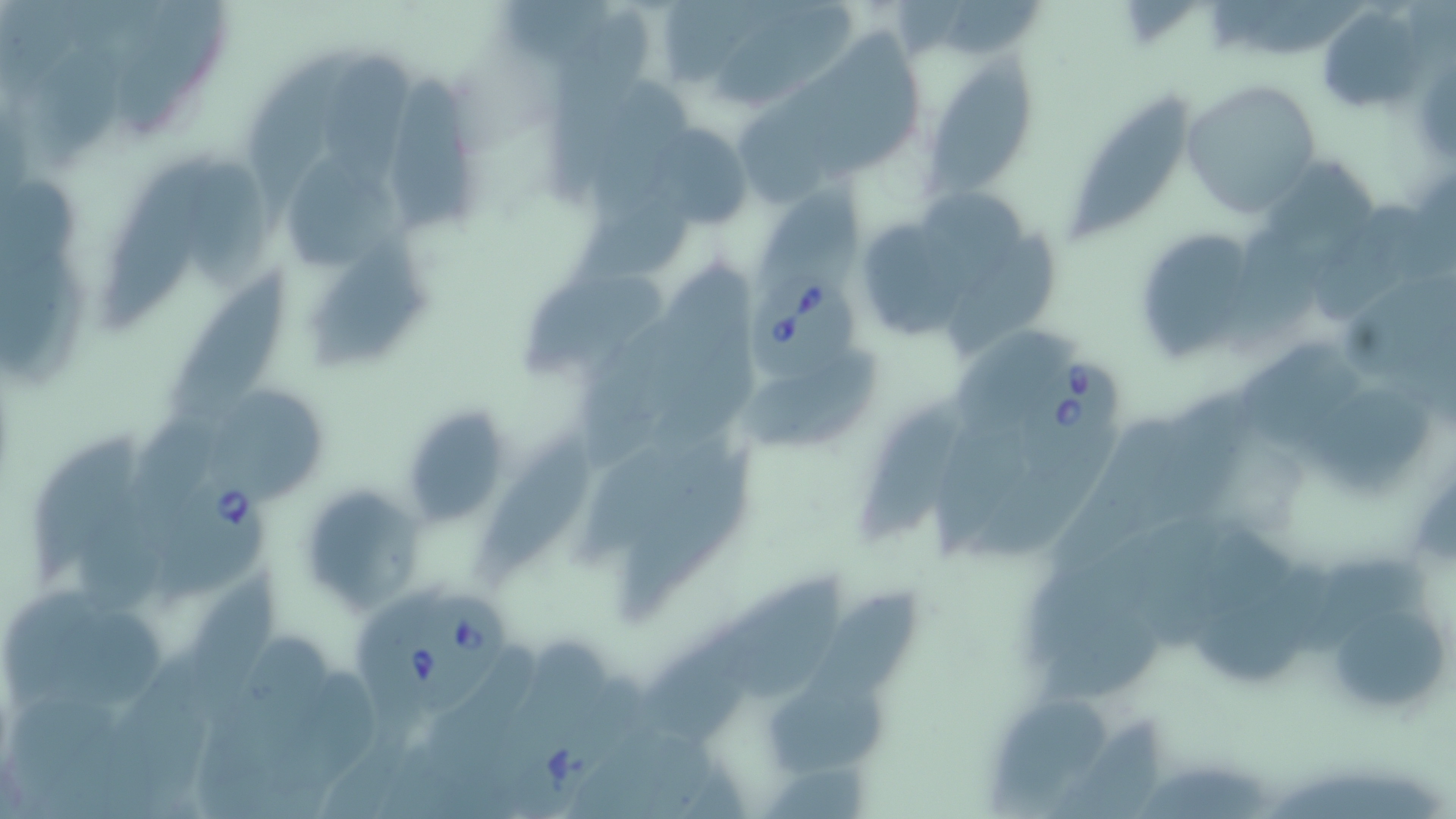
Summary:
  - Coordinate format: approximate bounding boxes as (x1,y1)-(x2,y2) corner pairs in pixels
  - Babesia divergens-infected red blood cell locations: (750,260)-(861,390), (1031,355)-(1120,465), (155,464)-(278,614), (396,591)-(505,723)
  - Uninfected red blood cell locations: (663,0)-(796,91), (1119,1)-(1197,49), (716,8)-(858,112), (1319,8)-(1427,117), (25,37)-(129,179), (321,53)-(411,199), (248,54)-(340,233), (923,57)-(1040,196), (386,77)-(480,231), (1182,79)-(1321,217), (585,81)-(698,221), (1067,96)-(1191,245), (642,122)-(755,232), (96,151)-(221,331), (289,151)-(400,272), (181,154)-(274,292), (759,178)-(866,292), (921,184)-(1031,291), (571,193)-(695,289), (862,223)-(966,336), (1132,226)-(1259,364), (306,231)-(432,374), (944,233)-(1060,358), (173,269)-(293,437), (520,271)-(666,375), (1235,339)-(1367,456), (729,351)-(886,458), (1310,385)-(1431,502), (200,386)-(321,500), (860,398)-(966,557), (398,406)-(513,527), (576,433)-(743,565), (33,435)-(140,589), (476,435)-(588,585), (619,454)-(760,625), (299,483)-(421,610), (186,568)-(283,736), (726,573)-(844,710), (803,590)-(920,713), (1187,591)-(1311,691), (6,592)-(105,719), (1321,609)-(1452,716), (44,611)-(167,715), (646,626)-(763,744), (771,685)-(893,777), (990,695)-(1110,805), (1047,709)-(1166,817)
  - Slide-level diagnosis: Babesia divergens
  - Stain: May-Grünwald-Giemsa
  - Preparation: thin blood smear
  - Modality: optical microscopy
  - Field of view: one of a larger specimen
  - Magnification: 1000x
  - Image size: 1456×819 pixels